Assess this cell for malaria.
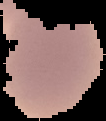

It is uninfected.

Image is 106×121 pixels. From a thin blood smear. Segmented cell region on a black background.